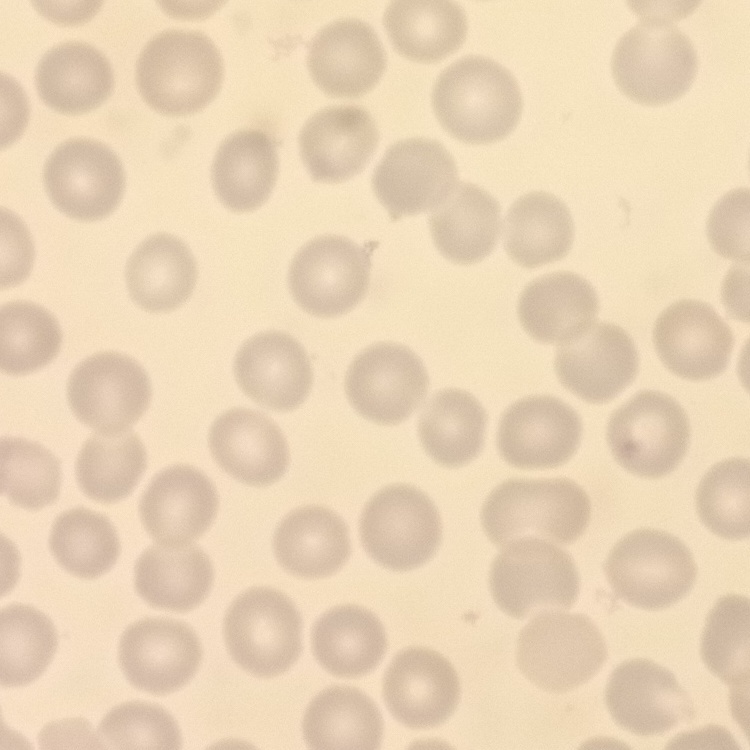 The red blood cells show no rouleaux formation. Thin blood smear. Field's or Giemsa stain. Square crop of a larger photomicrograph.